Outline each blood parasite and name the species.
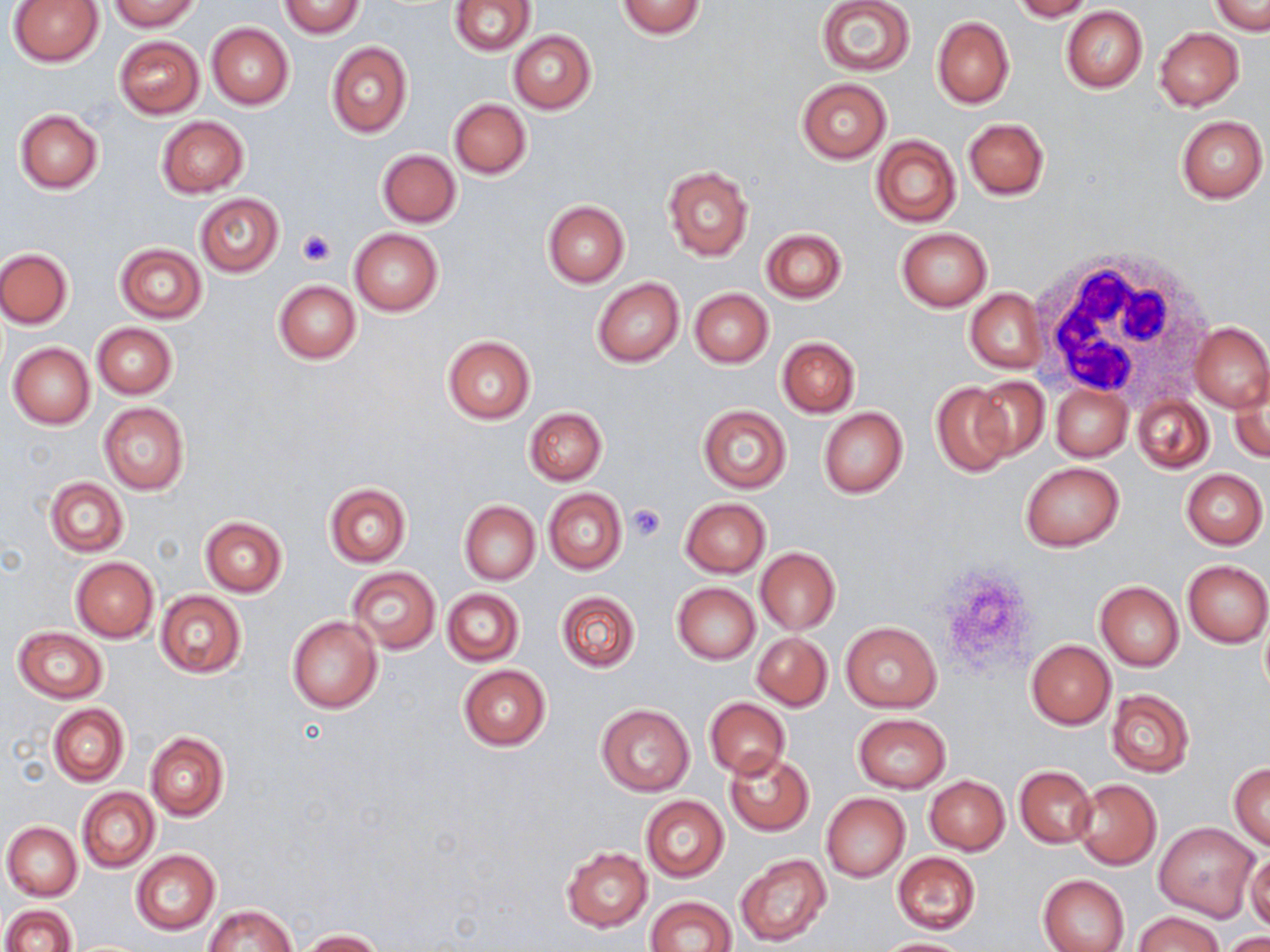

No blood parasites seen.

Approximate bounding boxes as (x1, y1, x2, y2) in pixels. Platelet locations: (296, 230, 334, 267), (625, 503, 666, 543). White blood cell locations: (1031, 249, 1218, 408). Uninfected red blood cell locations: (109, 0, 199, 31), (1010, 0, 1093, 21), (1210, 0, 1268, 36), (7, 1, 104, 66), (277, 1, 366, 38), (449, 1, 536, 55), (616, 1, 706, 38), (815, 1, 916, 77), (1061, 6, 1149, 93), (932, 17, 1014, 109), (206, 23, 293, 110), (1154, 27, 1244, 110), (508, 30, 596, 114), (115, 36, 204, 117), (325, 42, 413, 138), (796, 78, 891, 164), (449, 98, 531, 179), (14, 109, 103, 193), (1176, 115, 1268, 203), (156, 116, 248, 197), (963, 118, 1049, 199), (870, 134, 961, 228), (377, 149, 461, 228), (662, 165, 753, 261), (195, 194, 283, 276), (542, 201, 629, 287), (896, 227, 993, 311), (349, 228, 443, 315), (761, 228, 847, 303), (116, 243, 206, 323), (1, 248, 74, 328), (592, 277, 683, 367), (274, 280, 360, 364), (689, 288, 773, 368), (965, 289, 1047, 374), (92, 323, 177, 399), (1189, 323, 1270, 412), (442, 336, 535, 423), (776, 337, 860, 417), (7, 342, 95, 428), (1229, 368, 1270, 463), (971, 376, 1050, 458), (930, 383, 1014, 478), (1051, 384, 1131, 461), (1134, 394, 1213, 471), (98, 402, 189, 495), (697, 405, 791, 492), (524, 407, 606, 486), (818, 407, 907, 499), (1019, 462, 1124, 551), (1181, 468, 1267, 548), (44, 476, 129, 557), (324, 483, 410, 567), (543, 488, 625, 574), (680, 497, 771, 577), (459, 501, 540, 584), (199, 516, 287, 597), (756, 548, 839, 634), (71, 557, 158, 642), (1182, 560, 1270, 647), (345, 566, 439, 654), (1094, 581, 1184, 670), (672, 582, 759, 664), (441, 588, 523, 666), (154, 591, 246, 678), (555, 591, 640, 672), (287, 616, 383, 713), (839, 622, 942, 712), (12, 627, 107, 703), (752, 632, 832, 710), (1026, 640, 1114, 729), (458, 664, 551, 750), (1106, 689, 1194, 777), (705, 698, 789, 780), (49, 703, 129, 786), (596, 705, 694, 796), (853, 714, 951, 793), (146, 731, 228, 820), (724, 750, 813, 835), (1229, 763, 1270, 848), (1014, 765, 1096, 848), (925, 775, 1009, 855), (1072, 780, 1161, 869), (77, 787, 159, 873), (821, 793, 910, 882), (640, 795, 728, 882), (2, 821, 82, 901), (1154, 822, 1257, 920), (562, 846, 652, 931), (1245, 849, 1269, 932), (131, 850, 220, 934), (892, 852, 980, 933), (736, 853, 832, 947), (1038, 874, 1129, 952), (644, 896, 739, 952), (1, 904, 75, 952), (205, 904, 296, 952), (1135, 911, 1224, 952), (298, 929, 384, 951), (1221, 933, 1270, 952), (873, 938, 977, 952). Slide-level diagnosis: no evidence of blood parasites. May-Grünwald-Giemsa stain. Image is 1270×952 pixels. Captured at 1000x magnification. One field of a larger specimen. Thin blood smear. Light microscopy.